Name the blood parasite species.
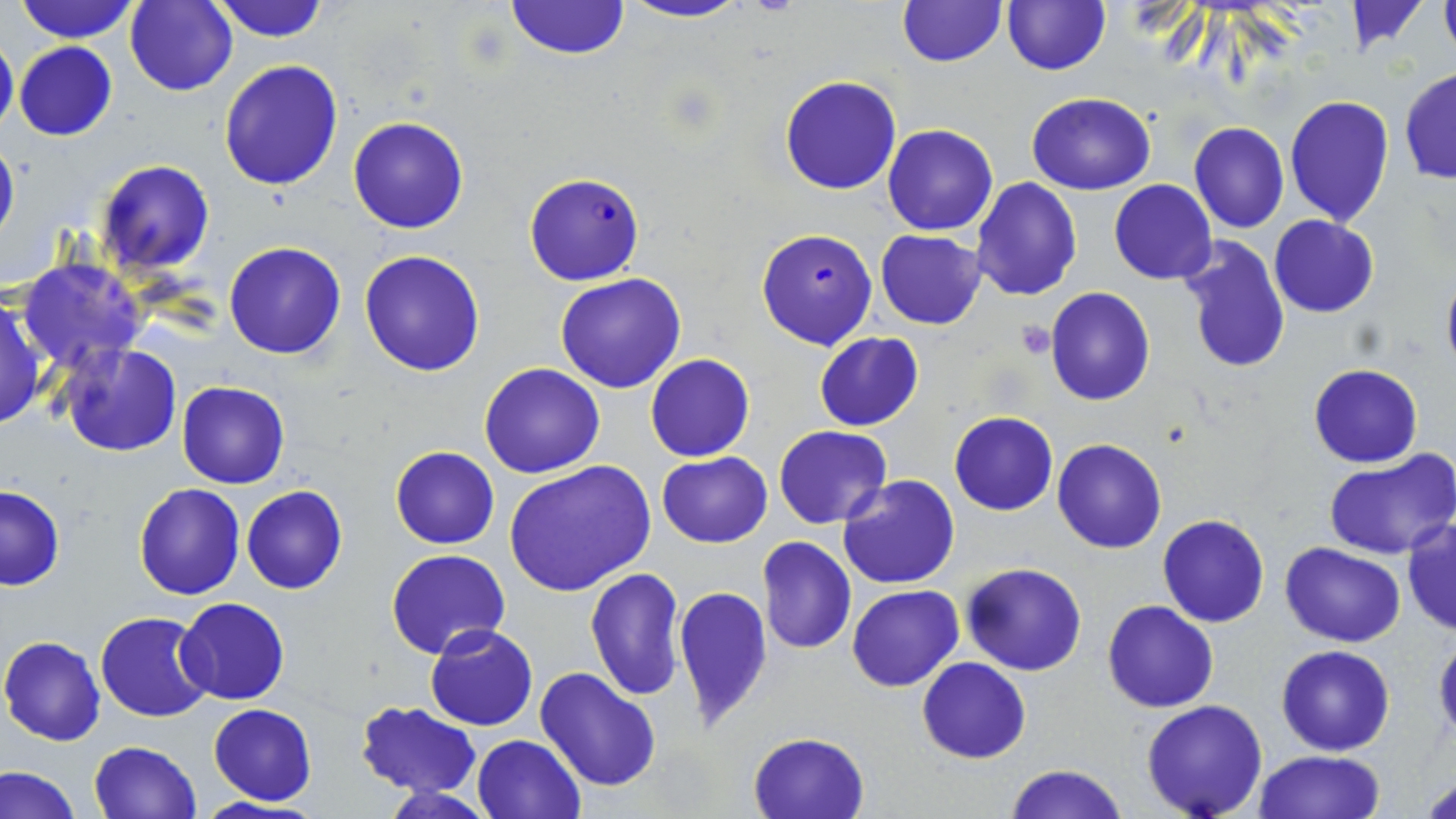

Plasmodium falciparum.

Approximate bounding boxes as named x1/y1/x2/y2 corners in pixels. Plasmodium falciparum-infected red blood cell locations: (x1=523, y1=173, x2=644, y2=285), (x1=759, y1=229, x2=880, y2=349). Uninfected red blood cell locations: (x1=14, y1=0, x2=140, y2=43), (x1=125, y1=0, x2=236, y2=95), (x1=211, y1=0, x2=329, y2=42), (x1=505, y1=0, x2=629, y2=60), (x1=619, y1=0, x2=753, y2=24), (x1=1001, y1=0, x2=1111, y2=75), (x1=1439, y1=0, x2=1456, y2=58), (x1=896, y1=1, x2=1008, y2=68), (x1=1336, y1=3, x2=1431, y2=54), (x1=0, y1=32, x2=18, y2=139), (x1=13, y1=41, x2=118, y2=140), (x1=218, y1=60, x2=343, y2=191), (x1=1400, y1=67, x2=1456, y2=184), (x1=779, y1=74, x2=903, y2=195), (x1=1027, y1=93, x2=1156, y2=194), (x1=1283, y1=95, x2=1395, y2=226), (x1=347, y1=115, x2=469, y2=234), (x1=1189, y1=121, x2=1289, y2=233), (x1=884, y1=124, x2=998, y2=234), (x1=0, y1=134, x2=20, y2=249), (x1=95, y1=159, x2=215, y2=275), (x1=972, y1=177, x2=1082, y2=300), (x1=1109, y1=180, x2=1217, y2=284), (x1=1269, y1=215, x2=1379, y2=318), (x1=875, y1=229, x2=986, y2=331), (x1=1176, y1=236, x2=1292, y2=375), (x1=224, y1=242, x2=346, y2=359), (x1=360, y1=249, x2=487, y2=376), (x1=17, y1=255, x2=146, y2=373), (x1=1439, y1=263, x2=1456, y2=378), (x1=554, y1=273, x2=686, y2=393), (x1=1046, y1=287, x2=1154, y2=405), (x1=0, y1=294, x2=49, y2=430), (x1=813, y1=331, x2=924, y2=432), (x1=56, y1=344, x2=182, y2=458), (x1=645, y1=354, x2=754, y2=462), (x1=1309, y1=363, x2=1423, y2=467), (x1=479, y1=364, x2=605, y2=478), (x1=177, y1=380, x2=289, y2=488), (x1=949, y1=411, x2=1058, y2=516), (x1=774, y1=425, x2=891, y2=529), (x1=1051, y1=438, x2=1167, y2=553), (x1=390, y1=446, x2=499, y2=549), (x1=656, y1=450, x2=773, y2=548), (x1=1325, y1=450, x2=1456, y2=562), (x1=505, y1=460, x2=658, y2=598), (x1=839, y1=473, x2=961, y2=590), (x1=133, y1=484, x2=245, y2=600), (x1=0, y1=485, x2=65, y2=592), (x1=241, y1=485, x2=347, y2=595), (x1=1158, y1=514, x2=1269, y2=627), (x1=1402, y1=517, x2=1455, y2=635), (x1=757, y1=537, x2=857, y2=655), (x1=1280, y1=542, x2=1405, y2=647), (x1=386, y1=549, x2=509, y2=659), (x1=962, y1=563, x2=1087, y2=676), (x1=582, y1=566, x2=685, y2=702), (x1=673, y1=583, x2=773, y2=730), (x1=846, y1=584, x2=963, y2=692), (x1=177, y1=598, x2=290, y2=704), (x1=1103, y1=601, x2=1217, y2=712), (x1=96, y1=612, x2=214, y2=722), (x1=425, y1=625, x2=539, y2=730), (x1=1, y1=634, x2=107, y2=746), (x1=1432, y1=634, x2=1455, y2=745), (x1=1276, y1=645, x2=1393, y2=756), (x1=916, y1=657, x2=1031, y2=763), (x1=535, y1=666, x2=661, y2=791), (x1=1141, y1=699, x2=1268, y2=819), (x1=355, y1=700, x2=481, y2=797), (x1=207, y1=702, x2=316, y2=805), (x1=748, y1=730, x2=870, y2=819), (x1=472, y1=733, x2=585, y2=818), (x1=88, y1=740, x2=202, y2=819), (x1=1254, y1=750, x2=1384, y2=819), (x1=0, y1=763, x2=81, y2=819), (x1=1005, y1=763, x2=1127, y2=819), (x1=1421, y1=771, x2=1456, y2=817), (x1=381, y1=783, x2=494, y2=817), (x1=194, y1=797, x2=324, y2=819). 1000x magnification. One field of a larger specimen. May-Grünwald-Giemsa stain. Image is 1456×819 pixels. Thin blood smear. Optical microscopy.